Describe the morphology of the red blood cells.
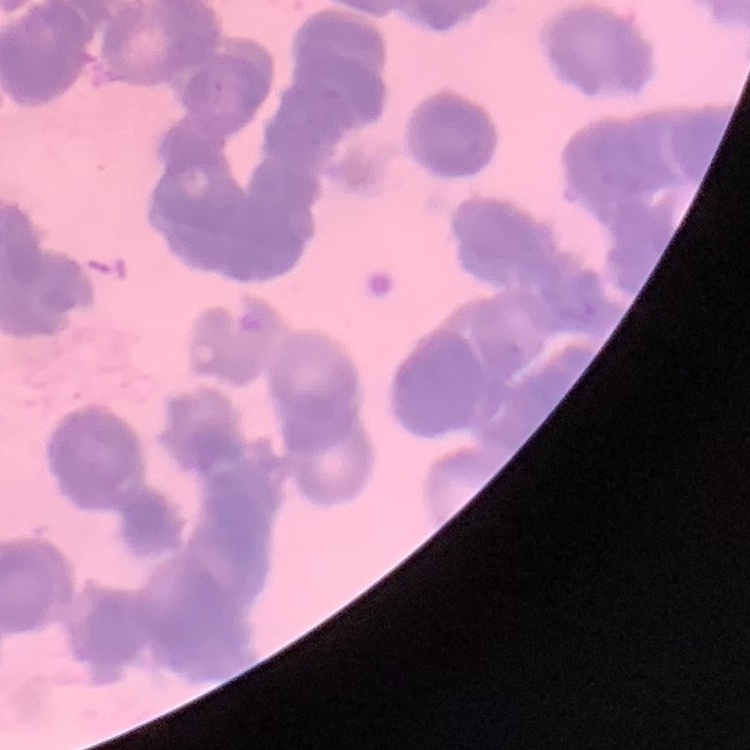

They show rouleaux formation.

One tile cut from a larger photomicrograph. Thin peripheral smear. Field's or Giemsa stain.